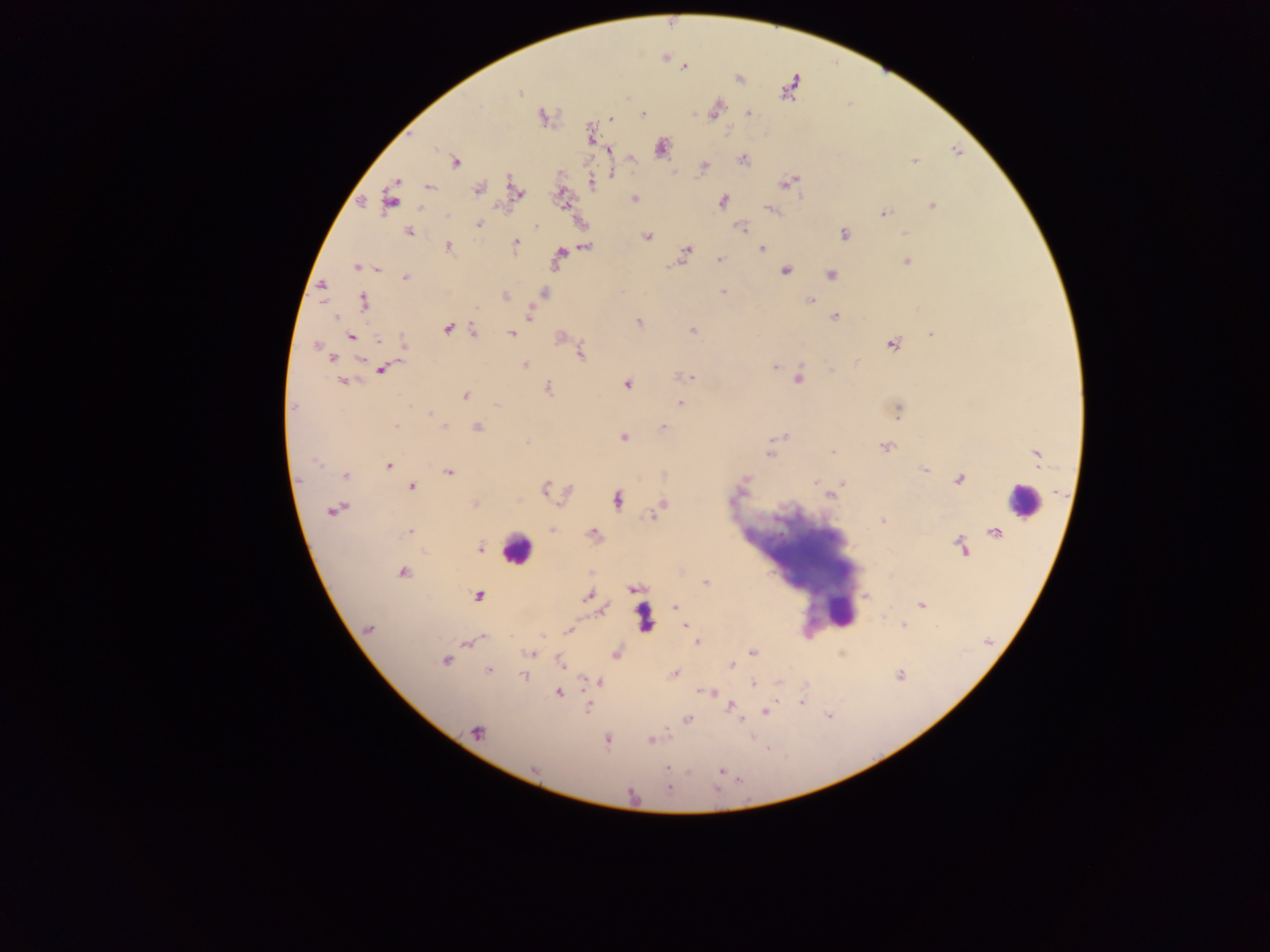 Approximate centers as [x, y] in pixels. Leukocyte locations: [1021, 500], [516, 550], [843, 612], [646, 617]. Plasmodium parasite locations: [685, 68], [519, 93], [714, 109], [749, 112], [643, 114], [542, 116], [612, 118], [661, 149], [608, 151], [632, 158], [744, 159], [915, 161], [457, 163], [703, 166], [614, 173], [788, 182], [592, 183], [430, 188], [478, 189], [517, 191], [562, 197], [634, 198], [389, 200], [722, 202], [932, 206], [770, 209], [884, 214], [448, 215], [479, 224], [536, 227], [742, 228], [408, 231], [906, 232], [844, 234], [648, 237], [516, 243], [586, 246], [448, 247], [761, 247], [687, 249], [560, 253], [719, 259], [906, 262], [355, 268], [378, 270], [785, 271], [830, 274], [405, 277], [322, 285], [722, 292], [544, 293], [505, 296], [810, 300], [364, 301], [529, 316], [834, 317], [335, 318], [638, 322], [448, 328], [473, 331], [692, 331], [511, 334], [931, 334], [352, 337], [561, 337], [380, 341], [405, 343], [893, 344], [316, 347], [581, 353], [332, 358], [361, 361], [857, 362], [524, 365], [774, 367], [383, 370], [831, 370], [683, 377], [691, 377], [798, 378], [343, 381], [626, 385], [548, 388], [463, 395], [680, 403], [496, 405], [293, 407], [898, 411], [431, 413], [396, 426], [444, 426], [663, 427], [477, 428], [782, 436], [622, 437], [527, 442], [886, 447], [832, 452], [769, 455], [1037, 455], [317, 461], [389, 466], [924, 469], [448, 473], [346, 476], [745, 479], [959, 479], [815, 482], [843, 483], [412, 487], [545, 488], [830, 495], [617, 500], [663, 503], [475, 505], [333, 510], [656, 519], [883, 521], [552, 529], [409, 531], [594, 532], [961, 546], [479, 548], [403, 573], [706, 583], [632, 589], [478, 595], [587, 596], [866, 597], [921, 605], [675, 607], [603, 610], [903, 625], [685, 626], [369, 628], [568, 631], [542, 635], [482, 638], [474, 641], [697, 642], [752, 652], [530, 654], [616, 654], [445, 659], [561, 663], [731, 666], [488, 670], [675, 674], [524, 675], [601, 681], [753, 683], [779, 683], [712, 692], [558, 693], [802, 703], [731, 706], [587, 708], [766, 712], [687, 719], [741, 722], [477, 732], [606, 738], [651, 740], [533, 768], [667, 768], [721, 771], [667, 789]. Mobile-phone photograph taken through the microscope. Sample from Ghana. One field of view. Image is 1270×952 pixels. Thick blood smear.